Report the malaria status of this cell.
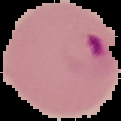

Parasitized.

image_size: 121×121 pixels
image_type: segmented cell region on a black background
preparation: thin blood smear